Report the malaria status of this cell.
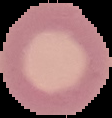
It is uninfected.

image type = segmented cell region on a black background
preparation = thin blood smear
image size = 112×118 pixels